Assess this cell for malaria.
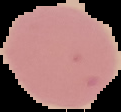

Uninfected.

{
  "image_size": "121×112 pixels",
  "preparation": "thin blood film",
  "image_type": "cell region segmented out of the field of view; surrounding area masked to black"
}